Assess this cell for malaria.
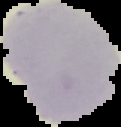

It is uninfected.

From a thin blood smear. Image is 121×127 pixels. Segmented cell region on a black background.